Report the malaria status of this cell.
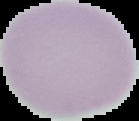

Uninfected.

{
  "image_type": "cell region segmented out of the field of view; surrounding area masked to black",
  "preparation": "thin blood smear",
  "image_size": "139×121 pixels"
}